Give the preparation type.
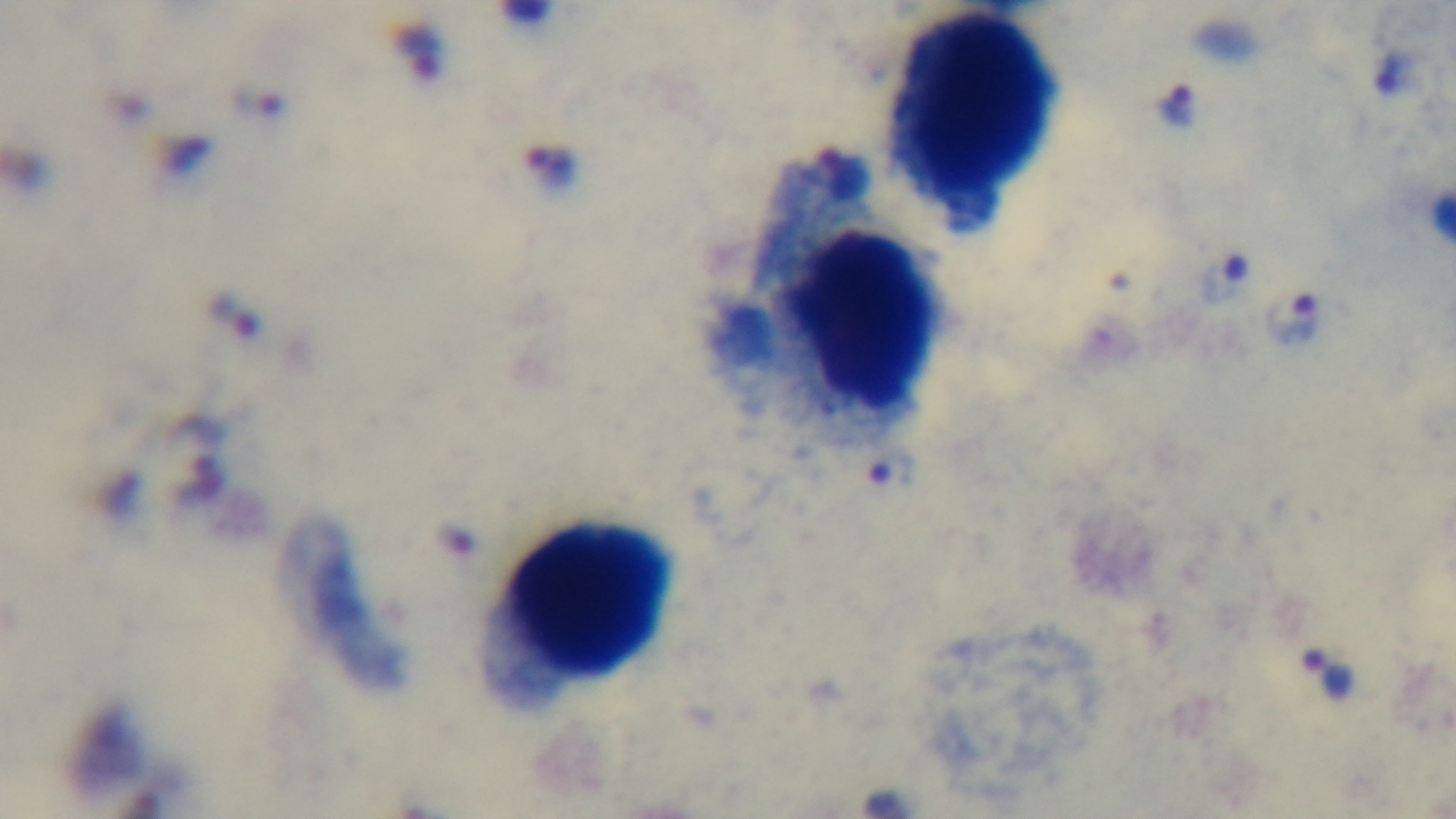
A thick smear.

Single field of view. 100x oil-immersion objective. Photomicrograph. Giemsa stain. Malaria status: positive. Captured with a mounted 4K digital camera.